Identify the parasite.
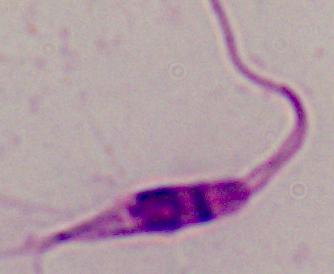
This is Leishmania.

modality: photomicrograph
magnification: 1000x